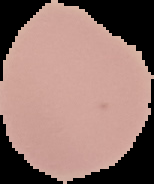 Image is 154×184 pixels. Result: no Plasmodium parasites detected. Segmented cell region on a black background. From a thin blood film.